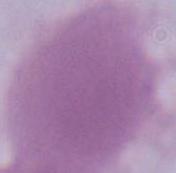

A red blood cell is shown. Photomicrograph. Captured at 1000x magnification.